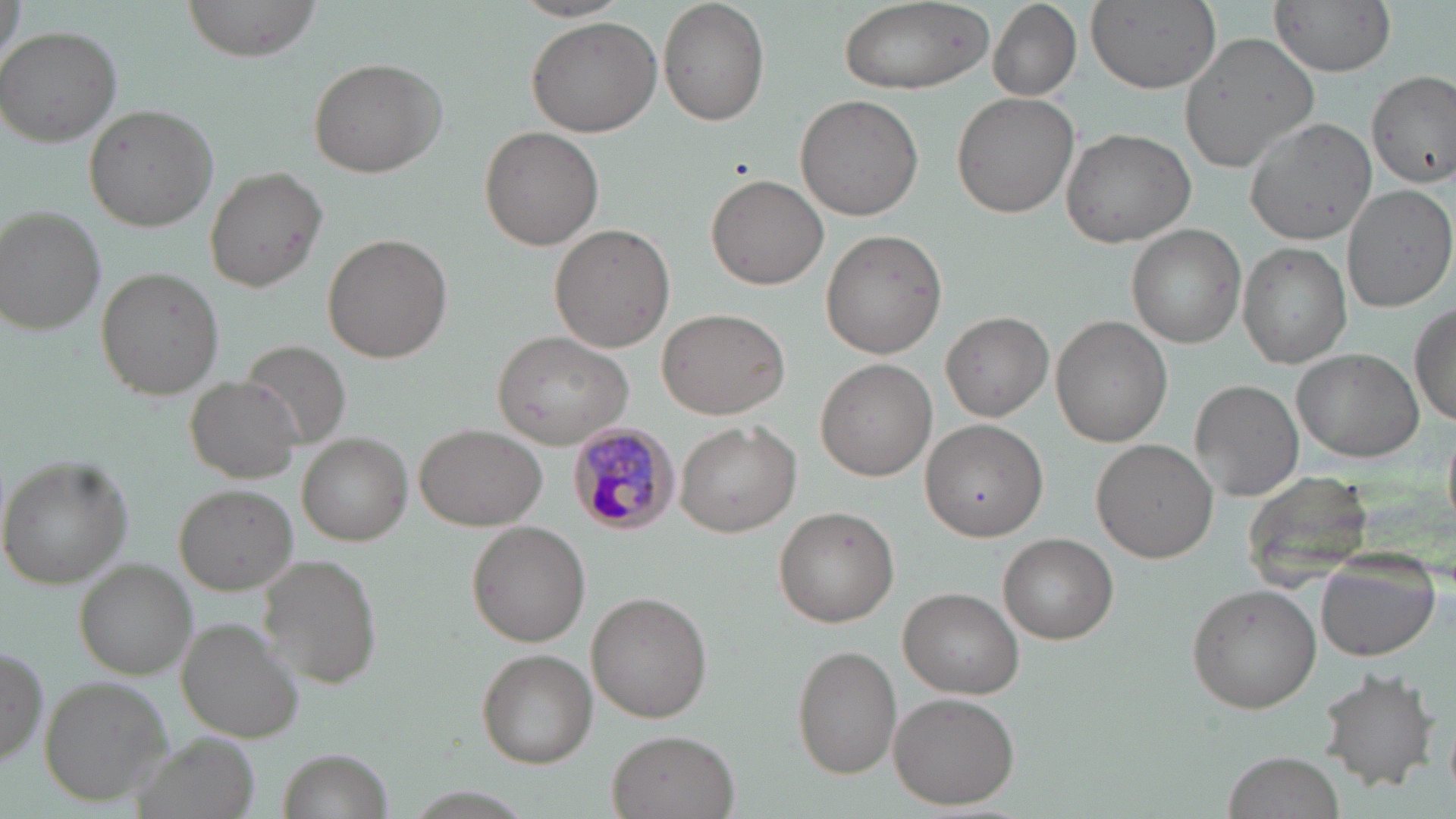 Approximate bounding boxes as named x1/y1/x2/y2 corners in pixels. Plasmodium malariae-infected red blood cell locations: (x1=569, y1=424, x2=683, y2=537). Uninfected red blood cell locations: (x1=1, y1=0, x2=26, y2=71), (x1=178, y1=0, x2=321, y2=62), (x1=837, y1=0, x2=995, y2=96), (x1=1085, y1=0, x2=1221, y2=92), (x1=1272, y1=0, x2=1396, y2=75), (x1=511, y1=1, x2=631, y2=23), (x1=658, y1=2, x2=770, y2=125), (x1=989, y1=3, x2=1082, y2=102), (x1=525, y1=18, x2=661, y2=136), (x1=1, y1=26, x2=123, y2=146), (x1=1178, y1=33, x2=1319, y2=173), (x1=309, y1=57, x2=446, y2=177), (x1=1366, y1=71, x2=1455, y2=187), (x1=952, y1=91, x2=1079, y2=217), (x1=796, y1=94, x2=923, y2=221), (x1=84, y1=104, x2=219, y2=232), (x1=1243, y1=117, x2=1377, y2=245), (x1=479, y1=126, x2=603, y2=250), (x1=1061, y1=127, x2=1196, y2=247), (x1=203, y1=167, x2=326, y2=292), (x1=706, y1=174, x2=829, y2=291), (x1=1343, y1=183, x2=1455, y2=314), (x1=1, y1=207, x2=106, y2=335), (x1=549, y1=224, x2=673, y2=352), (x1=1128, y1=225, x2=1245, y2=347), (x1=819, y1=229, x2=948, y2=360), (x1=325, y1=234, x2=453, y2=362), (x1=1238, y1=244, x2=1350, y2=368), (x1=96, y1=267, x2=225, y2=399), (x1=1412, y1=302, x2=1455, y2=430), (x1=657, y1=307, x2=790, y2=420), (x1=941, y1=311, x2=1053, y2=420), (x1=1051, y1=315, x2=1172, y2=446), (x1=493, y1=331, x2=632, y2=450), (x1=1293, y1=349, x2=1422, y2=460), (x1=815, y1=358, x2=937, y2=481), (x1=186, y1=375, x2=306, y2=483), (x1=1190, y1=378, x2=1303, y2=501), (x1=920, y1=420, x2=1049, y2=545), (x1=674, y1=421, x2=800, y2=536), (x1=415, y1=422, x2=546, y2=532), (x1=298, y1=434, x2=411, y2=545), (x1=1093, y1=437, x2=1221, y2=562), (x1=1, y1=457, x2=133, y2=588), (x1=1242, y1=470, x2=1376, y2=591), (x1=174, y1=484, x2=296, y2=595), (x1=773, y1=506, x2=900, y2=626), (x1=467, y1=520, x2=591, y2=648), (x1=998, y1=533, x2=1117, y2=644), (x1=1316, y1=550, x2=1441, y2=661), (x1=259, y1=554, x2=381, y2=687), (x1=77, y1=560, x2=192, y2=678), (x1=1186, y1=583, x2=1322, y2=712), (x1=899, y1=586, x2=1022, y2=697), (x1=587, y1=592, x2=712, y2=722), (x1=179, y1=616, x2=307, y2=743), (x1=791, y1=645, x2=901, y2=778), (x1=0, y1=646, x2=47, y2=769), (x1=475, y1=649, x2=597, y2=768), (x1=1319, y1=667, x2=1438, y2=791), (x1=39, y1=676, x2=171, y2=806), (x1=888, y1=691, x2=1022, y2=808), (x1=606, y1=729, x2=739, y2=819), (x1=281, y1=750, x2=386, y2=818), (x1=1223, y1=751, x2=1346, y2=819). Slide-level diagnosis: Plasmodium malariae. One field of a larger specimen. May-Grünwald-Giemsa stain. Captured at 1000x magnification. Light microscopy. Image is 1456×819 pixels. Thin blood film.